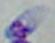

identification = Toxoplasma gondii
modality = micrograph
magnification = 1000x